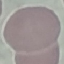

Malaria status: uninfected. Thin blood film. Automatically extracted cell patch, resized to 64 × 64 pixels. Giemsa stain. Acquired by smartphone through the microscope eyepiece.